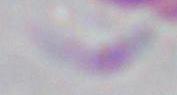

magnification = 1000x
identification = Toxoplasma gondii
modality = micrograph